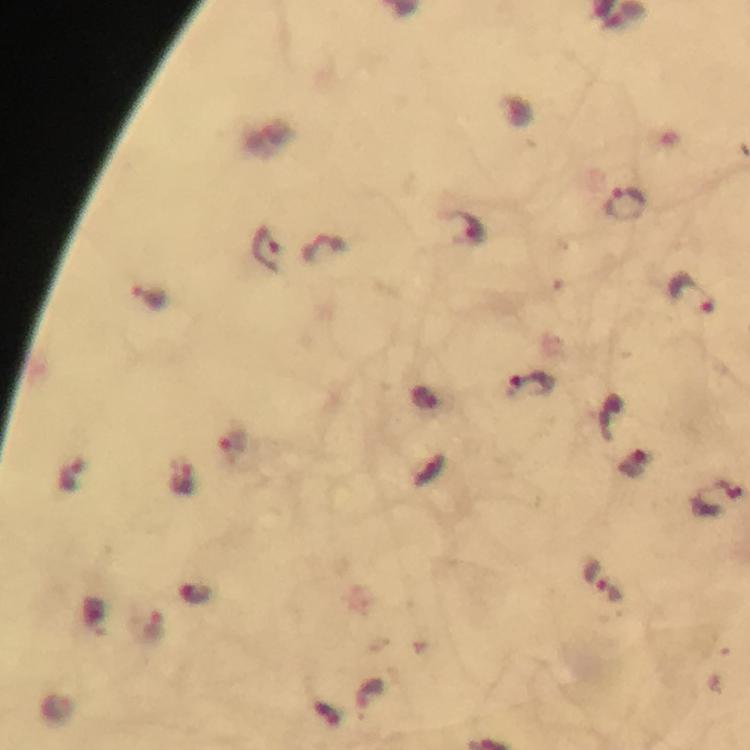

Approximate centers as [x, y] in pixels. Plasmodium parasite locations: [627, 204], [472, 228], [269, 251], [693, 294], [148, 298], [531, 387], [233, 446], [634, 465], [71, 476], [183, 477], [719, 498], [603, 581], [195, 595], [152, 628], [371, 692]. Immersion oil applied. Thick smear. Giemsa-stained preparation. Image is 750×750 pixels. Photographed through the microscope with a smartphone camera. From a malaria diagnostic workup. Cropped region of a single field of view. 100x magnification.